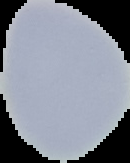

{
  "malaria_status": "uninfected",
  "image_size": "130×163 pixels",
  "image_type": "segmented cell region with the area outside set to black",
  "preparation": "thin blood smear"
}